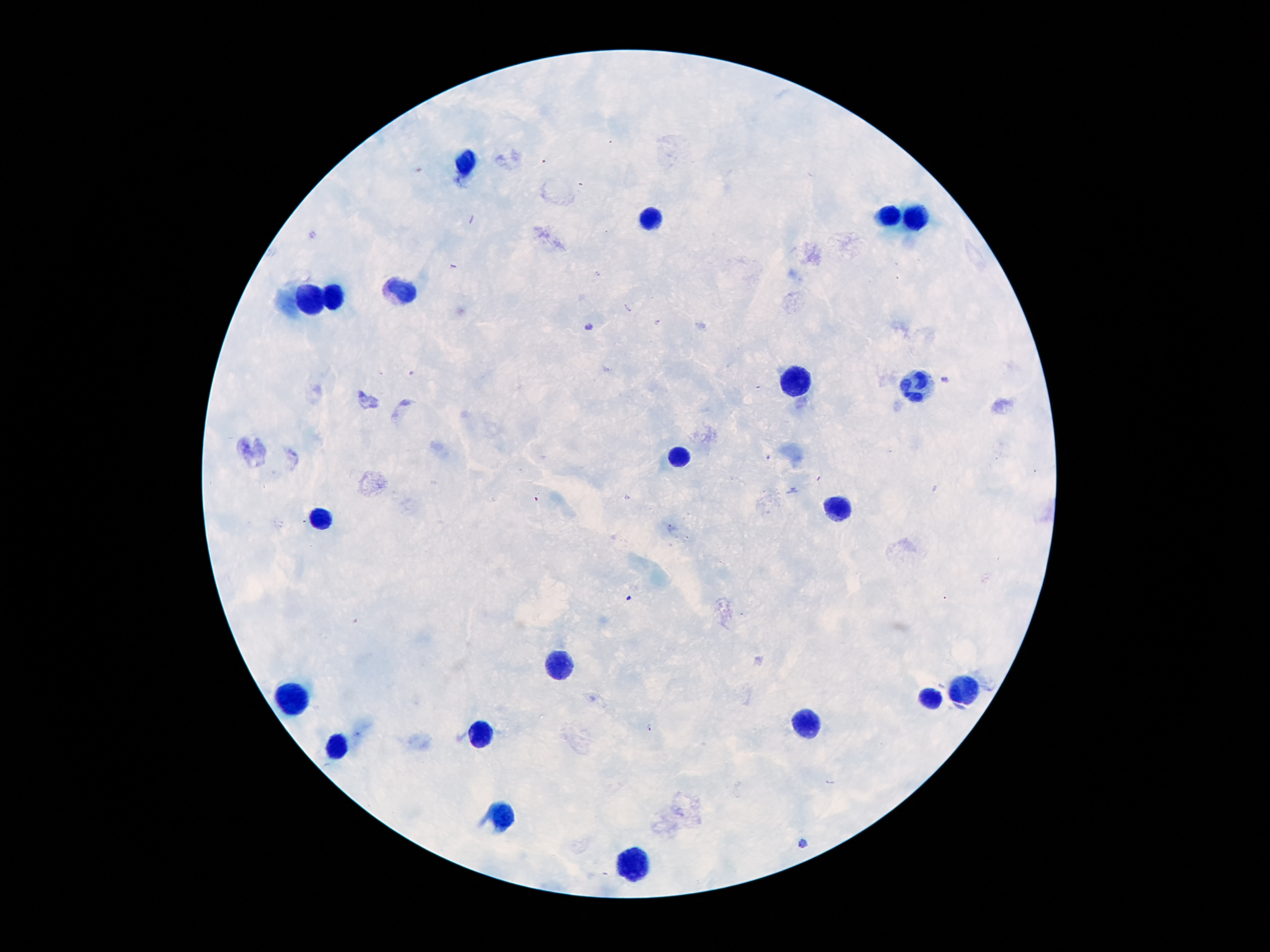

Approximate object centers, in pixels from the top-left corner.
Summary:
  - Plasmodium parasite locations: (x=590, y=327), (x=943, y=379), (x=650, y=727), (x=804, y=843)
  - Leukocyte locations: (x=466, y=160), (x=890, y=214), (x=651, y=219), (x=914, y=221), (x=399, y=293), (x=335, y=294), (x=309, y=301), (x=799, y=380), (x=915, y=385), (x=676, y=459), (x=835, y=510), (x=324, y=520), (x=554, y=666), (x=965, y=687), (x=287, y=698), (x=928, y=698), (x=802, y=729), (x=477, y=735), (x=338, y=744), (x=501, y=819), (x=629, y=864)
  - Field of view: one from this slide
  - Capture: smartphone through the microscope eyepiece
  - Image size: 1270×952 pixels
  - Patient malaria status: positive for Plasmodium falciparum
  - Stain: Giemsa
  - Preparation: thick blood smear
  - Magnification: 100x